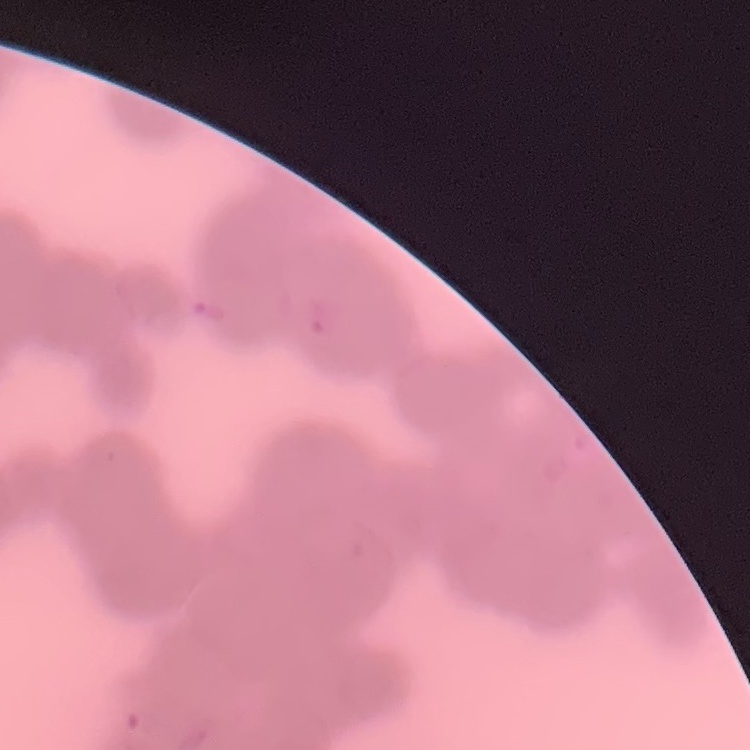
red blood cell morphology = rouleaux formation
image type = one tile cut from a larger photomicrograph
preparation = thin peripheral smear
stain = Field's or Giemsa